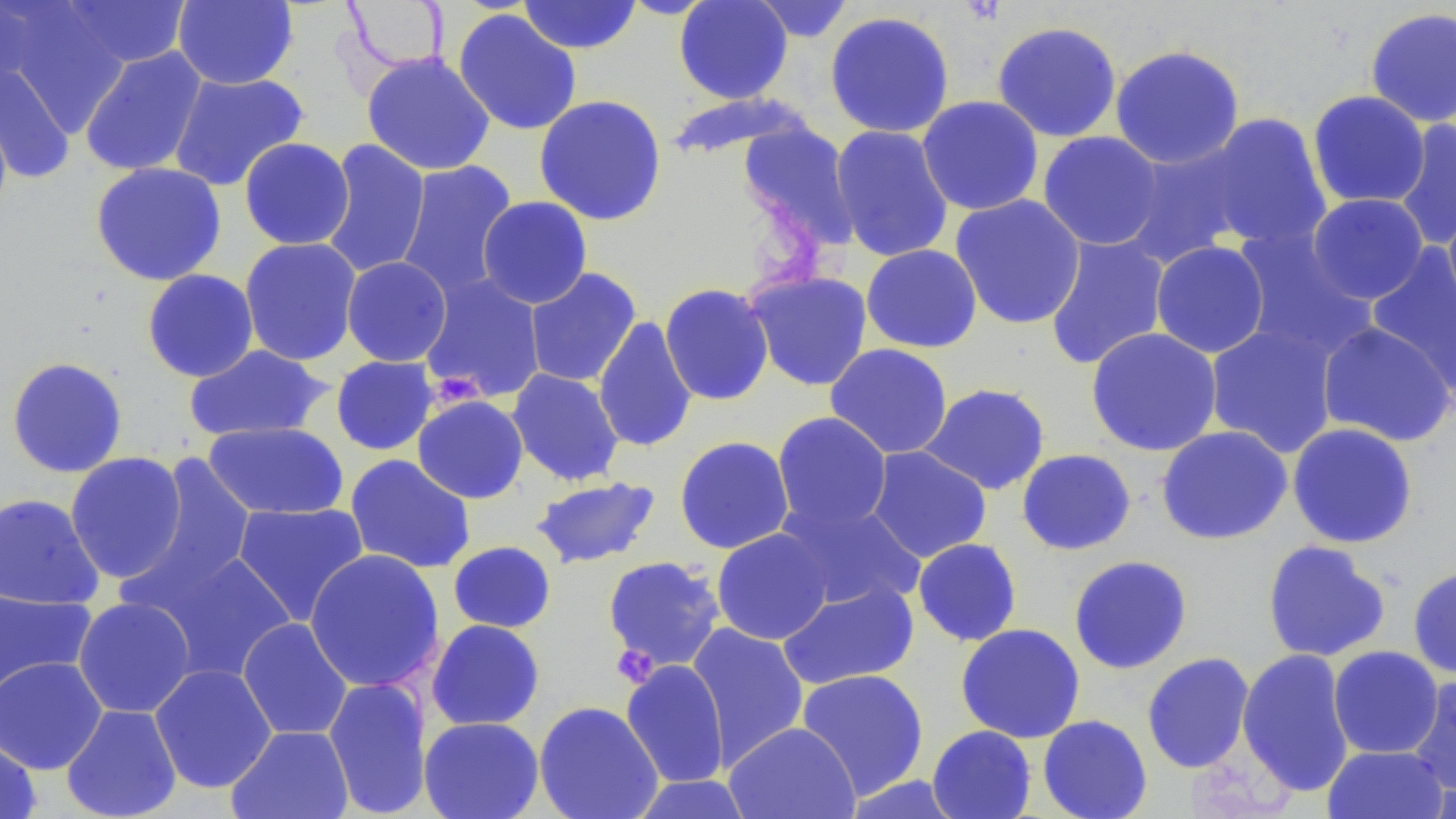

slide_level_diagnosis: no evidence of blood parasites
uninfected_red_blood_cell_locations: 'approximate bounding boxes as (x1, y1, x2, y2) in pixels: (0, 0, 51, 88), (58, 0, 191, 70), (172, 0, 299, 90), (518, 0, 642, 54), (674, 0, 793, 104), (748, 0, 856, 43), (340, 1, 453, 73), (4, 3, 132, 135), (1365, 7, 1456, 128), (452, 8, 582, 136), (824, 10, 956, 139), (991, 21, 1122, 142), (1109, 44, 1245, 170), (79, 46, 208, 177), (361, 52, 496, 176), (0, 61, 74, 183), (168, 70, 309, 192), (1306, 90, 1431, 209), (664, 92, 812, 162), (533, 94, 668, 226), (916, 95, 1044, 216), (0, 104, 13, 225), (1199, 112, 1333, 252), (1393, 118, 1456, 252), (737, 120, 860, 248), (830, 125, 955, 263), (1037, 131, 1164, 250), (239, 137, 355, 250), (319, 138, 431, 279), (1121, 142, 1252, 268), (394, 160, 519, 301), (90, 162, 227, 286), (950, 193, 1086, 330), (1307, 193, 1429, 304), (477, 196, 593, 309), (1442, 201, 1456, 323), (1232, 227, 1375, 361), (1044, 234, 1171, 371), (240, 237, 362, 365), (1151, 240, 1270, 358), (861, 244, 982, 353), (1365, 246, 1456, 394), (341, 256, 452, 367), (523, 268, 642, 388), (141, 269, 259, 382), (745, 270, 873, 391), (419, 274, 546, 403), (659, 283, 774, 406), (593, 317, 698, 453), (1317, 320, 1455, 447), (1205, 322, 1341, 459), (1085, 327, 1223, 457), (824, 343, 953, 459), (183, 344, 332, 443), (330, 355, 438, 456), (6, 356, 128, 478), (506, 368, 625, 487), (919, 383, 1051, 495), (412, 395, 529, 504), (771, 412, 892, 533), (202, 421, 349, 520), (1287, 422, 1418, 548), (1156, 425, 1293, 545), (674, 436, 795, 554), (866, 446, 992, 563), (1016, 448, 1136, 555), (64, 452, 188, 583), (130, 453, 257, 604), (344, 454, 476, 574), (529, 476, 661, 569), (0, 492, 104, 610), (776, 498, 925, 612), (232, 502, 369, 625), (711, 527, 834, 645), (912, 538, 1022, 647), (1261, 540, 1391, 663), (448, 541, 557, 633), (141, 547, 297, 683), (304, 550, 445, 692), (1068, 554, 1193, 674), (602, 556, 725, 672), (1407, 566, 1456, 678), (777, 580, 920, 690), (0, 586, 97, 700), (73, 597, 197, 718), (237, 617, 354, 740), (426, 619, 545, 731), (686, 622, 810, 767), (955, 623, 1085, 743), (1328, 645, 1443, 759), (1237, 648, 1355, 797), (1141, 652, 1255, 773), (0, 656, 108, 774), (621, 659, 730, 788), (149, 663, 277, 793), (796, 668, 930, 799), (1407, 673, 1456, 797), (322, 676, 433, 818), (533, 701, 664, 819), (60, 703, 182, 819), (1037, 714, 1153, 819), (419, 716, 544, 819), (724, 722, 860, 819), (227, 724, 354, 819), (927, 725, 1037, 818), (0, 736, 41, 819), (1323, 744, 1448, 819), (628, 774, 756, 818), (841, 774, 966, 818)'
magnification: 1000x
field_of_view: single
image_size: 1456×819 pixels
stain: May-Grünwald-Giemsa
platelet_locations: 'approximate bounding boxes as (x1, y1, x2, y2) in pixels: (432, 372, 491, 412), (611, 644, 658, 687)'
preparation: thin blood film
modality: optical microscopy